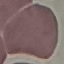

Malaria status: uninfected. Photographed with a smartphone camera at the microscope eyepiece. Thin smear of blood. Giemsa stain. Cell patch, automatically extracted from a larger field of view and resized to 64 × 64 pixels.